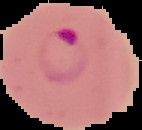
preparation = thin blood smear
malaria status = parasitized
image type = segmented cell region on a black background
image size = 142×130 pixels